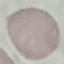

Malaria status: uninfected. Photographed with a smartphone camera at the microscope eyepiece. Thin blood smear. Cell patch, automatically extracted from a larger field of view and resized to 64 × 64 pixels. Giemsa stain.